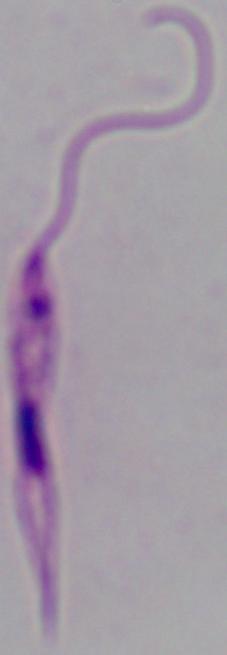 Captured at 1000x magnification. Micrograph. A Leishmania parasite is shown.